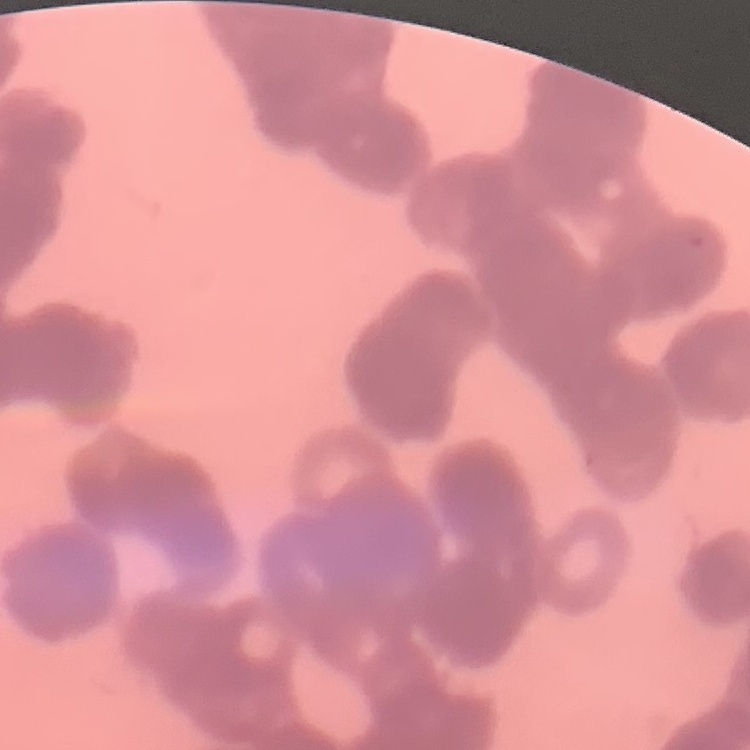
The red blood cells show rouleaux formation. One tile cut from a larger photomicrograph. Field's or Giemsa stain. Thin blood film.